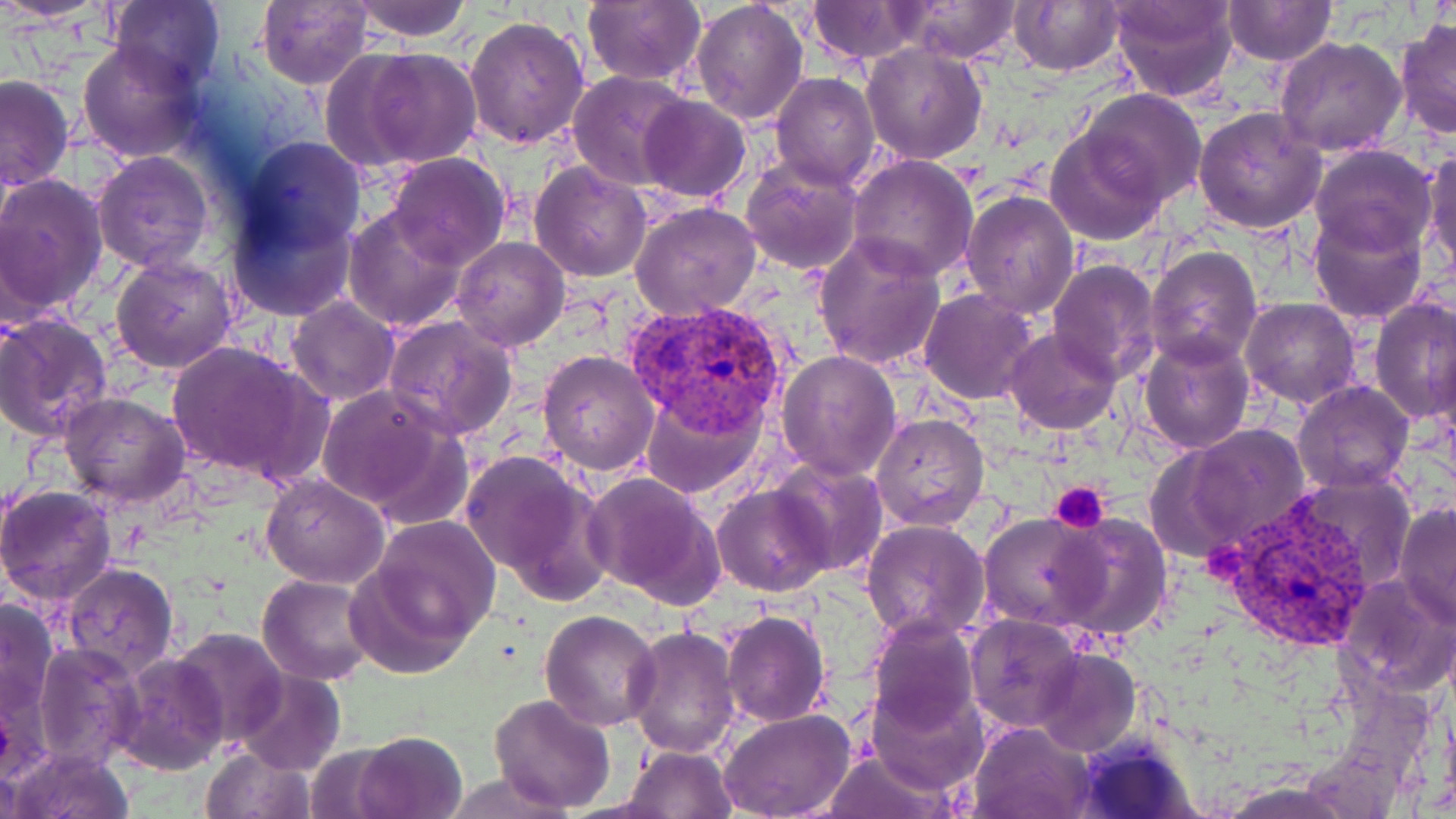
{
  "slide_level_diagnosis": "Plasmodium vivax",
  "platelet_locations": "approximate bounding boxes as (x1, y1, x2, y2) in pixels: (1049, 481, 1112, 532), (1199, 538, 1248, 584)",
  "plasmodium_vivax_infected_red_blood_cell_locations": "approximate bounding boxes as (x1, y1, x2, y2) in pixels: (624, 298, 789, 431), (1217, 494, 1387, 650)",
  "modality": "optical microscopy",
  "field_of_view": "one of a larger specimen",
  "image_size": "1456×819 pixels",
  "stain": "May-Grünwald-Giemsa",
  "uninfected_red_blood_cell_locations": "approximate bounding boxes as (x1, y1, x2, y2) in pixels: (4, 0, 111, 27), (107, 0, 226, 91), (583, 0, 706, 87), (690, 0, 809, 126), (897, 0, 1023, 63), (1008, 0, 1125, 76), (1108, 0, 1239, 103), (254, 1, 373, 89), (350, 1, 475, 42), (808, 1, 926, 62), (1221, 1, 1336, 67), (463, 15, 590, 149), (1394, 18, 1455, 140), (1274, 34, 1407, 156), (77, 40, 204, 162), (861, 43, 988, 165), (347, 47, 485, 169), (568, 71, 693, 191), (772, 72, 880, 190), (0, 75, 74, 191), (1079, 89, 1206, 207), (638, 95, 751, 204), (1193, 107, 1326, 233), (1045, 132, 1166, 245), (223, 136, 363, 306), (1308, 144, 1439, 260), (1421, 148, 1455, 278), (91, 152, 213, 274), (384, 153, 509, 270), (848, 154, 979, 282), (740, 156, 864, 276), (529, 161, 652, 282), (0, 174, 107, 321), (960, 189, 1080, 320), (630, 202, 762, 320), (342, 205, 470, 333), (1309, 208, 1430, 325), (812, 234, 947, 373), (451, 237, 570, 352), (1145, 244, 1264, 371), (111, 253, 238, 372), (1047, 260, 1161, 385), (919, 290, 1039, 405), (1370, 294, 1455, 426), (1240, 295, 1361, 408), (284, 296, 399, 406), (0, 313, 113, 442), (382, 314, 519, 440), (1004, 326, 1122, 435), (1138, 334, 1255, 454), (165, 339, 327, 486), (537, 349, 660, 477), (776, 349, 903, 481), (1293, 380, 1415, 494), (315, 385, 464, 519), (640, 390, 766, 497), (57, 391, 191, 510), (872, 413, 990, 531), (1166, 424, 1312, 554), (459, 449, 608, 596), (772, 459, 888, 578), (583, 472, 725, 606), (260, 473, 390, 589), (0, 484, 119, 606), (712, 484, 835, 597), (1394, 502, 1456, 627), (978, 510, 1105, 631), (1045, 511, 1173, 641), (362, 517, 500, 659), (860, 520, 989, 644), (62, 562, 179, 675), (1337, 572, 1456, 698), (257, 574, 378, 686), (0, 595, 60, 733), (540, 609, 663, 731), (720, 611, 831, 728), (866, 613, 978, 736), (963, 613, 1085, 733), (625, 625, 741, 758), (170, 628, 288, 745), (35, 640, 143, 770), (1033, 648, 1140, 758), (115, 653, 226, 772), (233, 668, 345, 776), (864, 685, 986, 796), (489, 694, 616, 811), (719, 709, 856, 819), (966, 720, 1096, 819), (352, 731, 470, 819), (303, 742, 402, 818), (200, 744, 316, 818), (8, 745, 135, 819), (622, 745, 736, 818), (819, 749, 955, 819), (442, 774, 568, 818)",
  "magnification": "1000x",
  "preparation": "thin blood smear"
}